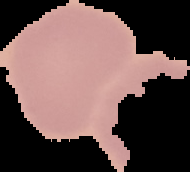 Malaria status: uninfected. Cell region segmented out of the field of view; the surrounding area is masked to black. From a thin blood smear. Image is 190×172 pixels.